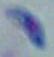
identification = Toxoplasma gondii
modality = micrograph
magnification = 1000x